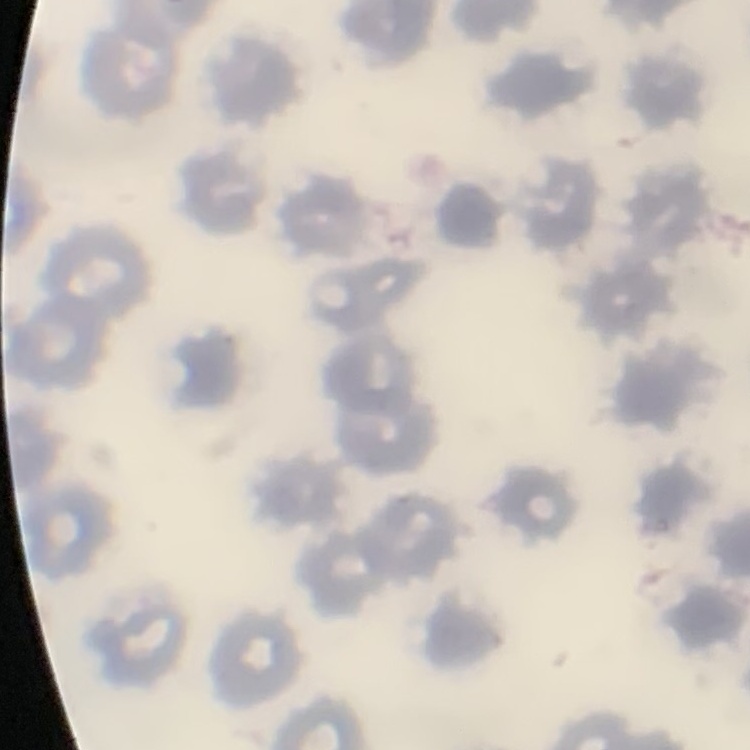
red blood cell morphology = no rouleaux formation
stain = Field's or Giemsa
image type = square crop of a larger photomicrograph
preparation = thin blood film